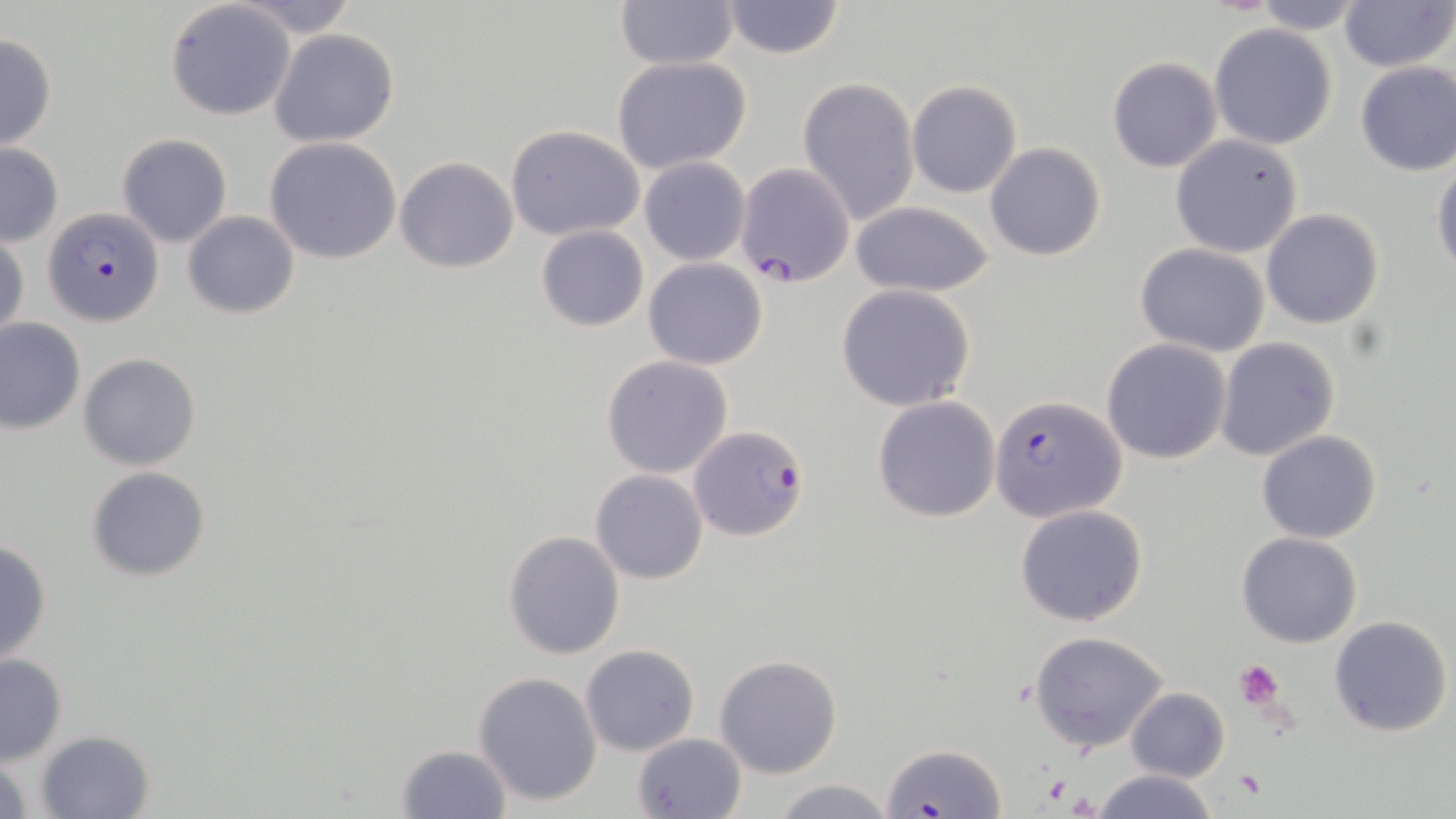

slide-level diagnosis = Plasmodium falciparum
image size = 1456×819 pixels
magnification = 1000x
Plasmodium falciparum-infected red blood cell locations = approximate bounding boxes as (x1, y1, x2, y2) in pixels: (734, 162, 855, 287), (43, 207, 166, 327), (990, 393, 1128, 524), (688, 423, 811, 542), (881, 744, 1004, 817)
platelet locations = approximate bounding boxes as (x1, y1, x2, y2) in pixels: (1235, 660, 1286, 709), (1234, 769, 1268, 800)
uninfected red blood cell locations = approximate bounding boxes as (x1, y1, x2, y2) in pixels: (232, 0, 361, 37), (614, 0, 740, 70), (1338, 0, 1453, 71), (165, 1, 296, 121), (718, 1, 847, 59), (1247, 1, 1368, 34), (1209, 23, 1338, 150), (268, 28, 401, 148), (0, 31, 57, 152), (611, 56, 752, 172), (1106, 57, 1222, 173), (1354, 61, 1456, 176), (796, 77, 919, 225), (907, 80, 1022, 198), (505, 125, 645, 241), (117, 133, 233, 247), (1171, 134, 1303, 258), (263, 137, 404, 264), (984, 142, 1106, 262), (0, 144, 64, 246), (394, 157, 520, 273), (639, 158, 750, 265), (1431, 161, 1456, 278), (849, 202, 996, 298), (1261, 208, 1385, 330), (182, 210, 300, 319), (534, 225, 650, 332), (1, 233, 28, 347), (1134, 243, 1269, 356), (643, 258, 768, 370), (836, 285, 977, 412), (0, 318, 86, 435), (1215, 337, 1340, 463), (1102, 338, 1232, 464), (79, 352, 202, 471), (601, 355, 734, 478), (872, 396, 1001, 522), (1257, 430, 1383, 545), (85, 466, 213, 583), (590, 469, 709, 584), (1014, 504, 1148, 627), (503, 530, 626, 659), (1235, 531, 1362, 648), (0, 538, 53, 665), (1327, 614, 1453, 738), (1027, 631, 1171, 755), (579, 644, 700, 756), (713, 653, 842, 777), (0, 654, 68, 765), (472, 671, 603, 808), (1125, 688, 1230, 781), (35, 729, 154, 817), (629, 732, 747, 819), (394, 744, 512, 819), (0, 751, 34, 817), (1090, 770, 1221, 819), (768, 778, 900, 819)
stain = May-Grünwald-Giemsa
field of view = one of a larger specimen
modality = light microscopy
preparation = thin blood smear